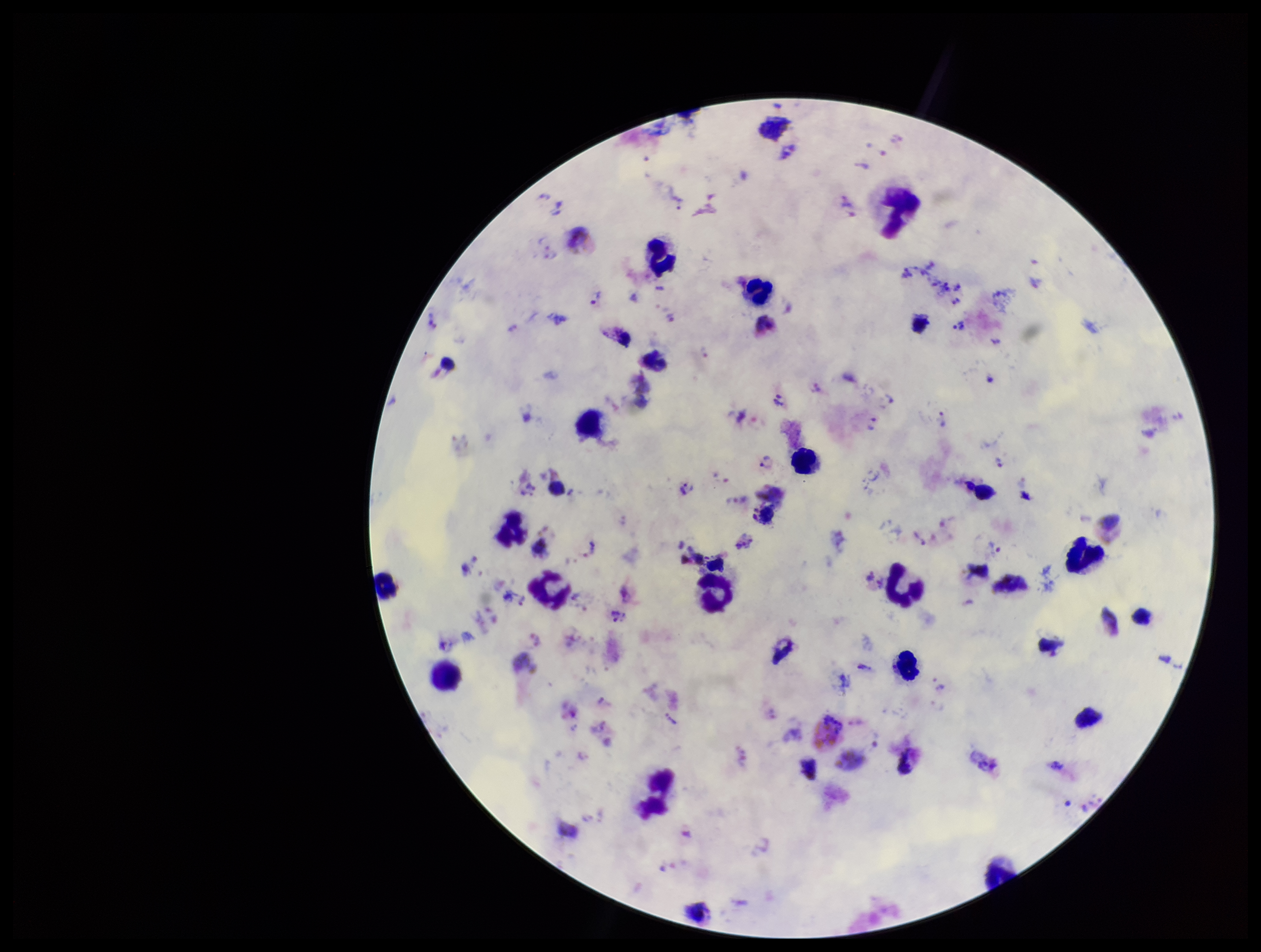

Parasite count: 47. Preparation: thick. One field from this slide. Leukocyte count: 18. Patient malaria status: infected. Plasmodium parasites: seen. Species reported for this patient: Plasmodium vivax. Smartphone photograph taken through the eyepiece of a microscope. Giemsa stain. Image is 1261×952 pixels.